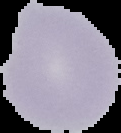

Image is 121×133 pixels. From a thin blood smear. Result: negative for malaria parasites. Segmented cell region on a black background.